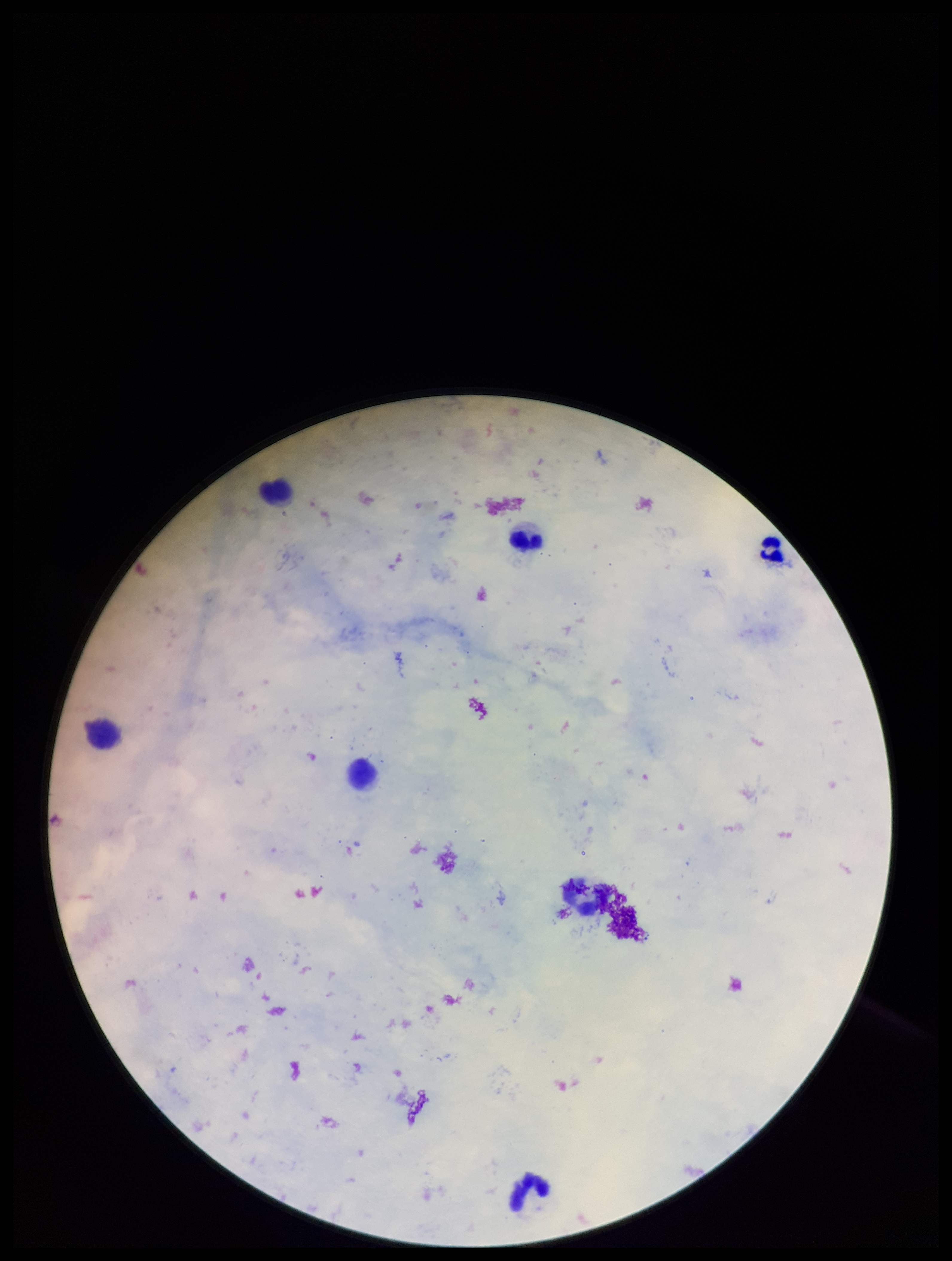
stain: Giemsa
capture: smartphone photograph through the microscope eyepiece
image_size: 952×1261 pixels
leukocyte_count: 5
plasmodium_parasites: none detected
field_of_view: one from this slide
patient_malaria_status: negative
preparation: thick
parasite_count: 0